Report the malaria status of this cell.
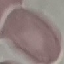

It is uninfected.

Giemsa-stained preparation. Acquired by smartphone through the microscope eyepiece. Automatically extracted cell patch, resized to 64 × 64 pixels. Thin blood film.